Assess the morphology of the erythrocytes.
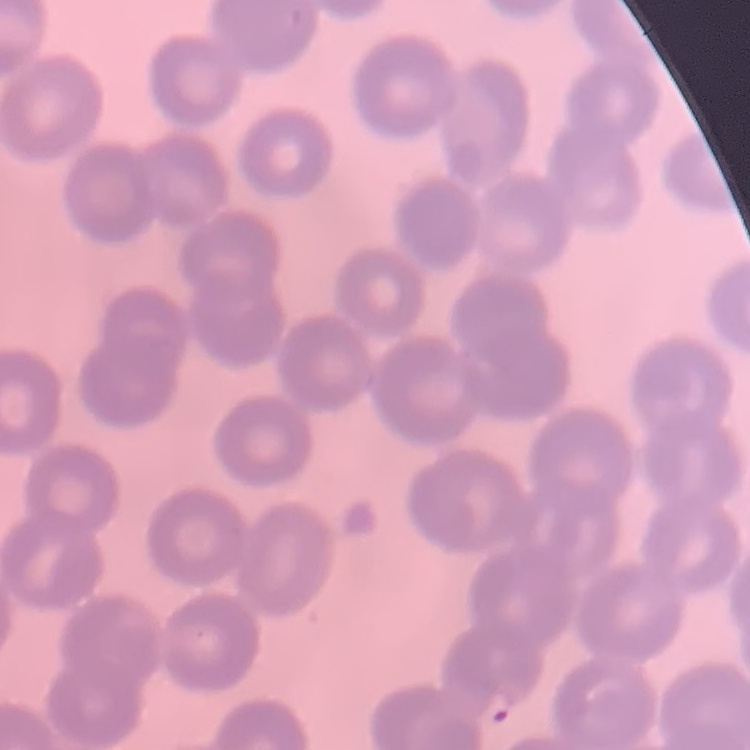
No rouleaux formation.

Summary:
  - Preparation: thin peripheral smear
  - Image type: one tile cut from a larger photomicrograph
  - Stain: Field's or Giemsa